Name the parasite shown.
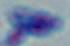

Toxoplasma gondii.

modality = micrograph
magnification = 1000x